Report the malaria status of this cell.
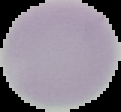

Uninfected.

Summary:
  - Image type: segmented cell region with the area outside set to black
  - Preparation: thin blood film
  - Image size: 121×112 pixels